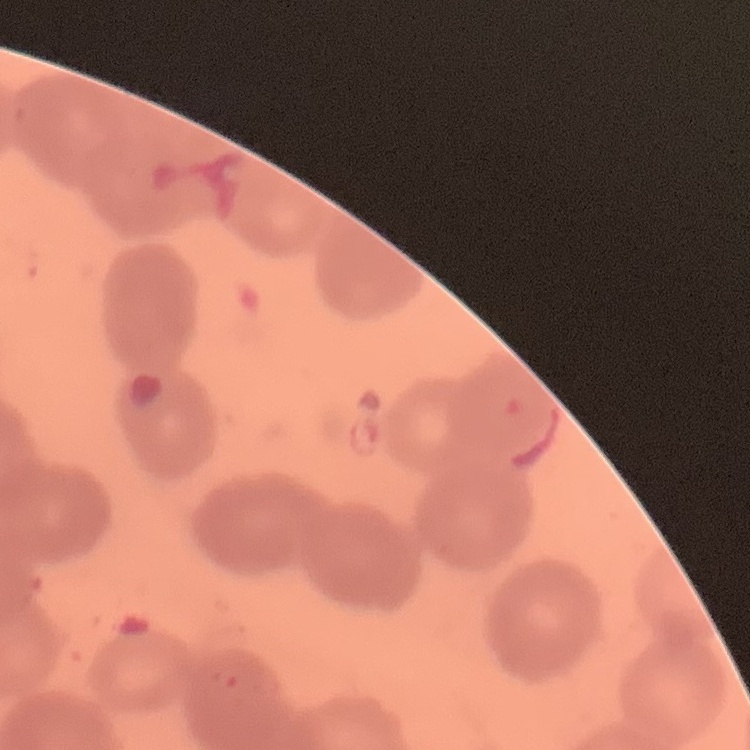

red blood cell morphology = rouleaux formation
stain = Field's or Giemsa
image type = square crop of a larger photomicrograph
preparation = thin peripheral smear